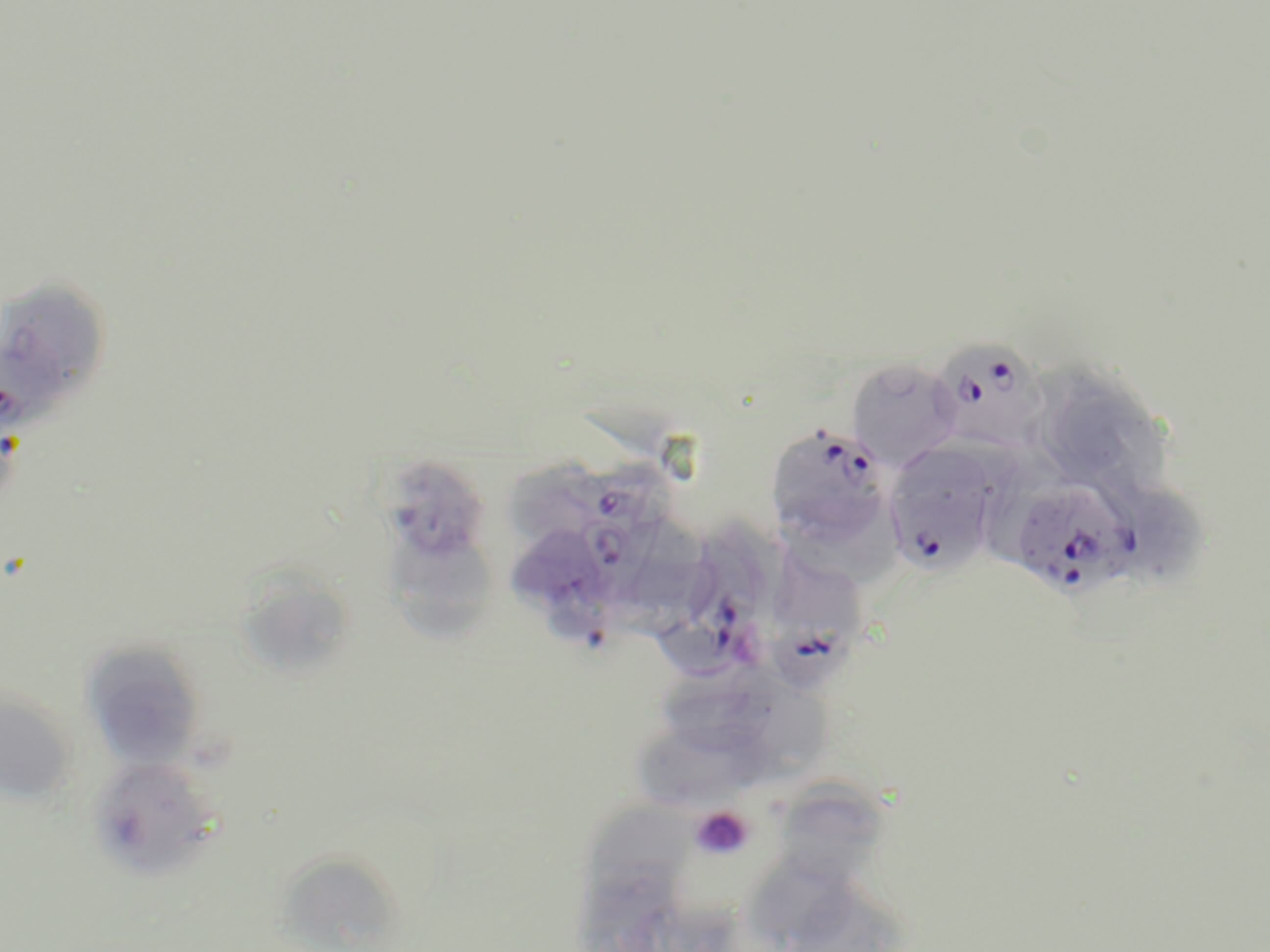
{
  "slide_level_diagnosis": "Plasmodium falciparum",
  "modality": "light microscopy",
  "image_size": "1270×952 pixels",
  "platelet_locations": "approximate bounding boxes as named x1/y1/x2/y2 corners in pixels: (x1=690, y1=806, x2=754, y2=860)",
  "uninfected_red_blood_cell_locations": "approximate bounding boxes as named x1/y1/x2/y2 corners in pixels: (x1=0, y1=276, x2=115, y2=421), (x1=846, y1=358, x2=962, y2=470), (x1=1058, y1=376, x2=1174, y2=493), (x1=506, y1=452, x2=596, y2=541), (x1=392, y1=462, x2=492, y2=556), (x1=1106, y1=468, x2=1211, y2=584), (x1=383, y1=526, x2=498, y2=642), (x1=507, y1=532, x2=613, y2=659), (x1=238, y1=562, x2=350, y2=680), (x1=80, y1=640, x2=208, y2=770), (x1=664, y1=663, x2=773, y2=749), (x1=731, y1=663, x2=837, y2=785), (x1=0, y1=686, x2=78, y2=805), (x1=643, y1=723, x2=750, y2=811), (x1=85, y1=755, x2=223, y2=881), (x1=784, y1=785, x2=882, y2=877), (x1=594, y1=801, x2=690, y2=910), (x1=281, y1=856, x2=408, y2=952), (x1=754, y1=856, x2=866, y2=942), (x1=573, y1=860, x2=685, y2=952), (x1=800, y1=897, x2=897, y2=952)",
  "field_of_view": "one of a larger specimen",
  "stain": "May-Grünwald-Giemsa",
  "plasmodium_falciparum_infected_red_blood_cell_locations": "approximate bounding boxes as named x1/y1/x2/y2 corners in pixels: (x1=934, y1=339, x2=1045, y2=449), (x1=765, y1=423, x2=893, y2=546), (x1=883, y1=449, x2=1000, y2=576), (x1=558, y1=452, x2=689, y2=536), (x1=1011, y1=481, x2=1139, y2=597), (x1=573, y1=516, x2=644, y2=604), (x1=660, y1=542, x2=759, y2=679), (x1=768, y1=550, x2=869, y2=696)",
  "preparation": "thin blood film",
  "magnification": "1000x"
}